Give the position of each P. falciparum parasite with its life-cycle stage, each leukocyte, and any debris.
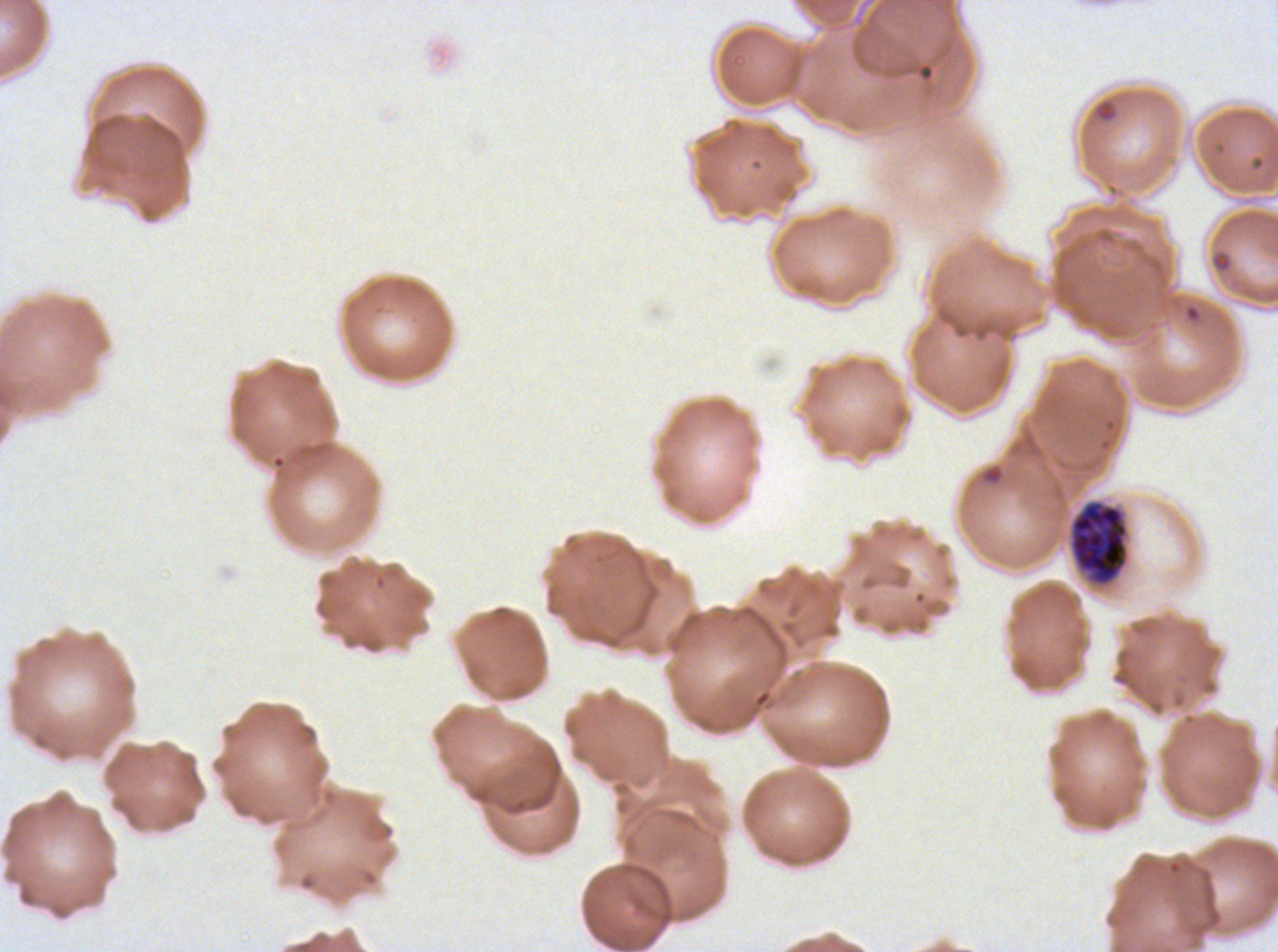

Approximate bounding boxes as {x1, y1, x2, y2} in pixels.
Rings: {1094, 100, 1117, 123}, {1184, 304, 1201, 323}.
Early schizonts: {1070, 502, 1128, 584}.
Debris: {1212, 254, 1232, 272}.
No late-ring/early-trophozoite forms, mid trophozoites, late trophozoites, late schizonts, segmenters, gametocytes, or leukocytes observed.

{
  "preparation": "thin blood smear",
  "field_of_view": "sub-image separated from a larger composite",
  "specimen": "P. falciparum from a patient in The Gambia, cultured ex vivo for 24 to 48 hours",
  "stain": "Giemsa",
  "life_cycle_stages_observed": "ring, early schizont",
  "image_size": "1278×952 pixels"
}